Look for Plasmodium parasites.
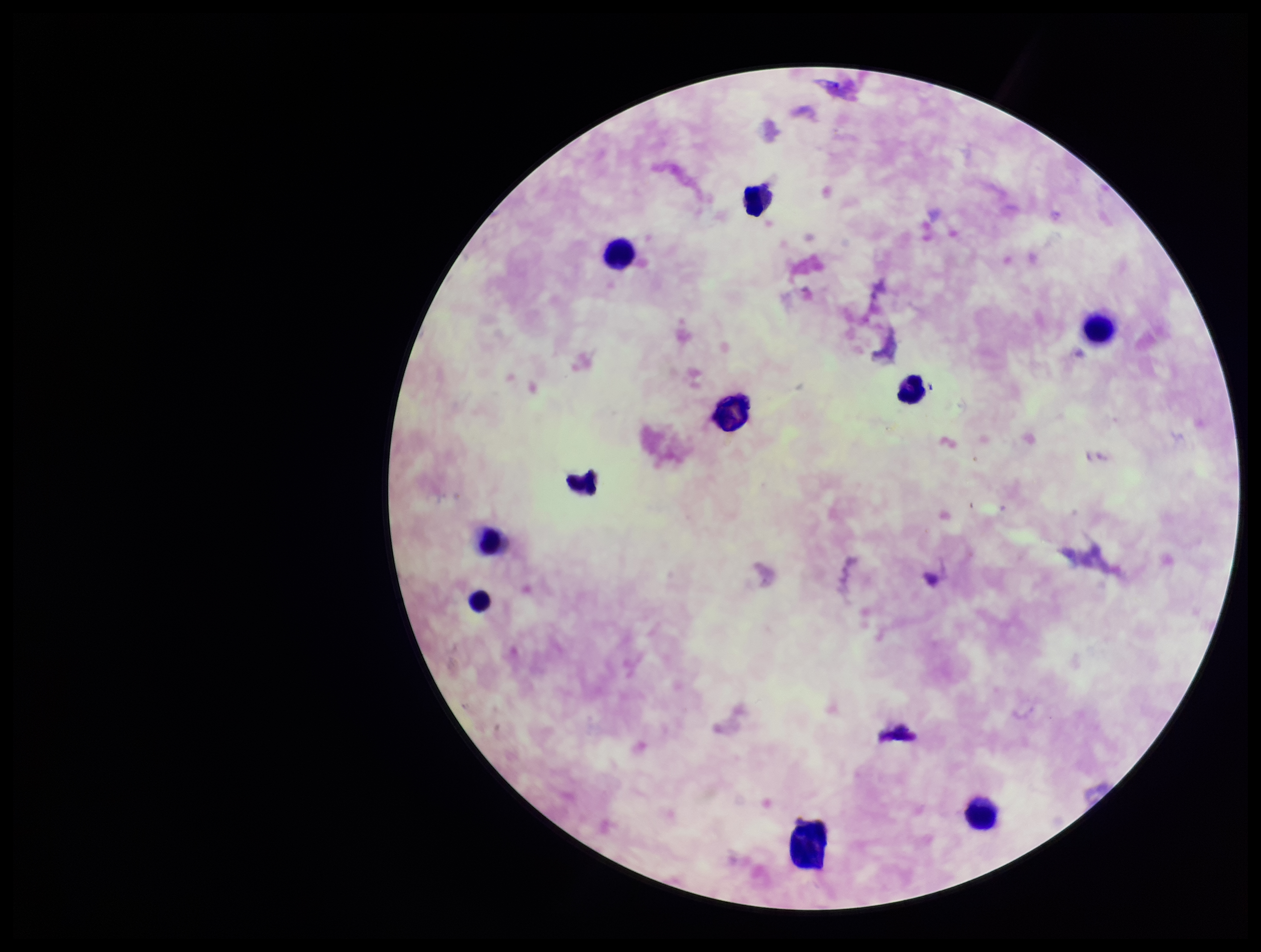

None seen.

Preparation: thick. Patient malaria status: positive. Image is 1261×952 pixels. Photographed through the microscope eyepiece with a smartphone camera. Leukocyte count: 9. One field from this slide. Parasite count: 0. Species reported for this patient: Plasmodium falciparum. Giemsa stain.